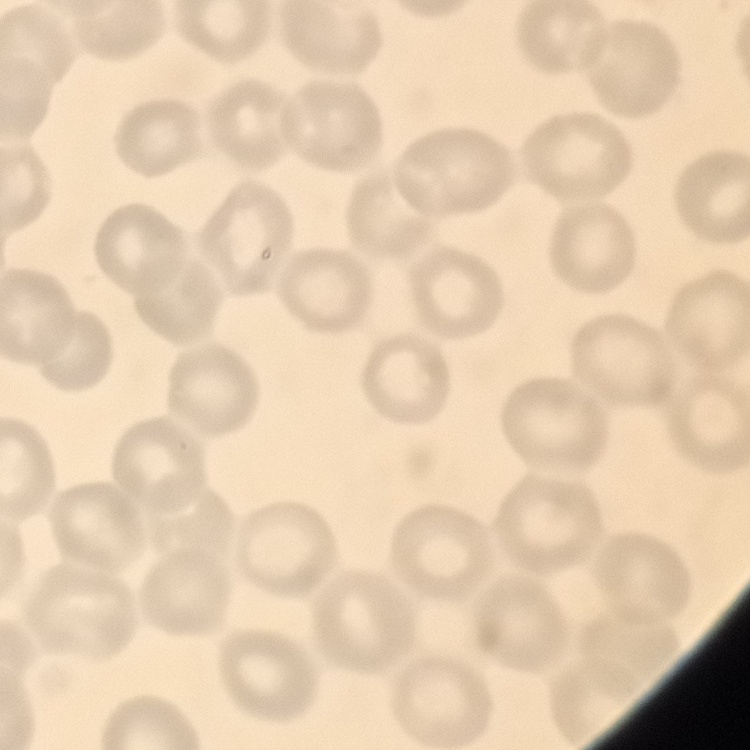

Summary:
  - Red blood cell morphology: no rouleaux formation
  - Preparation: thin peripheral smear
  - Image type: square crop of a larger photomicrograph
  - Stain: Field's or Giemsa